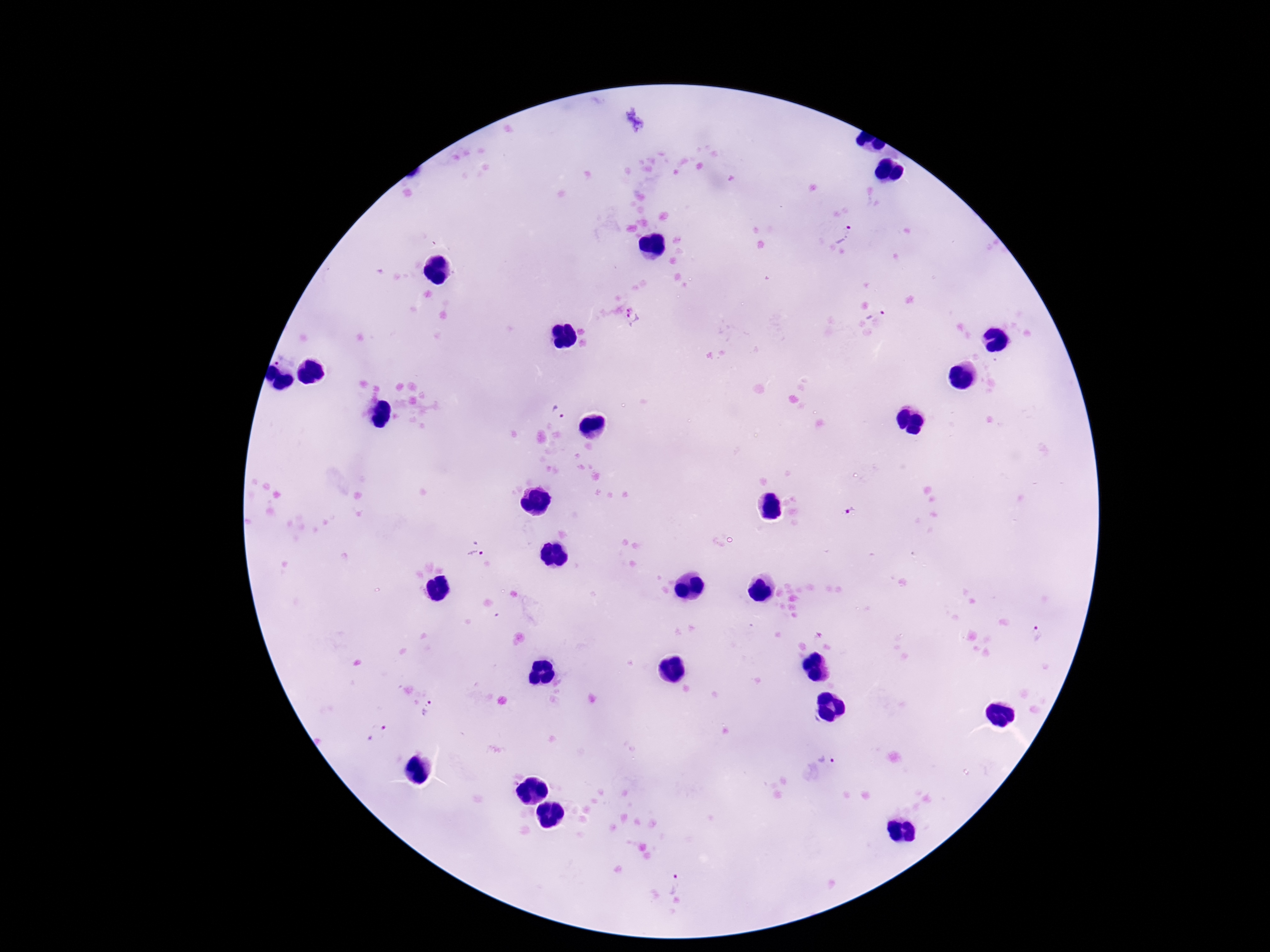

capture = smartphone camera through the microscope eyepiece
image size = 1270×952 pixels
patient malaria status = infected
magnification = 100x
stain = Giemsa
preparation = thick blood film
Plasmodium parasite locations = approximate centers as {x, y} in pixels: {843, 234}, {876, 309}, {633, 316}, {278, 357}, {560, 412}, {849, 509}, {475, 549}, {1037, 632}, {428, 709}, {377, 733}, {826, 759}, {676, 884}
field of view = single